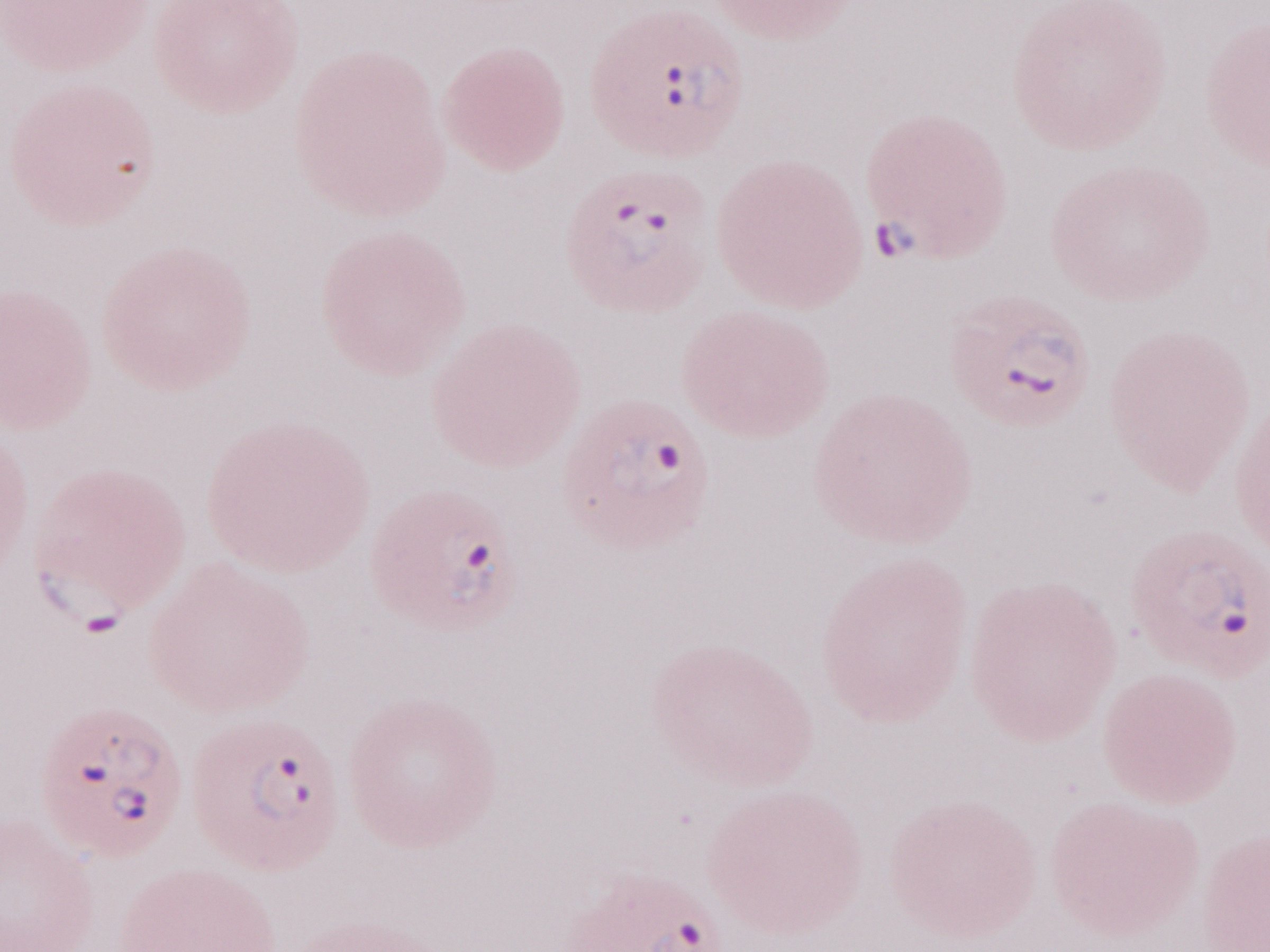 Magnification: 1,000x. Olympus BX43 microscope, Olympus DP73 camera. May-Grünwald-Giemsa-stained preparation. Single field of view. Image is 1270×952 pixels. Patient diagnosis: malaria infection. Thin peripheral-blood smear.